Identify the parasite.
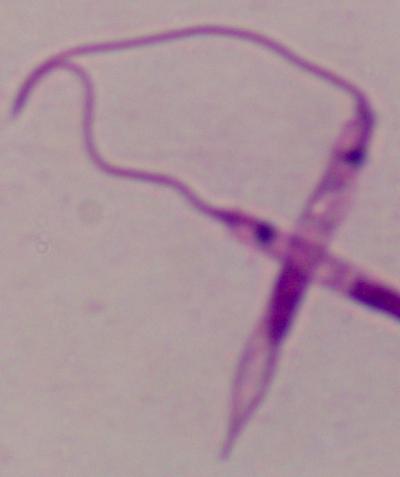
This is Leishmania.

1000x magnification. Photomicrograph.